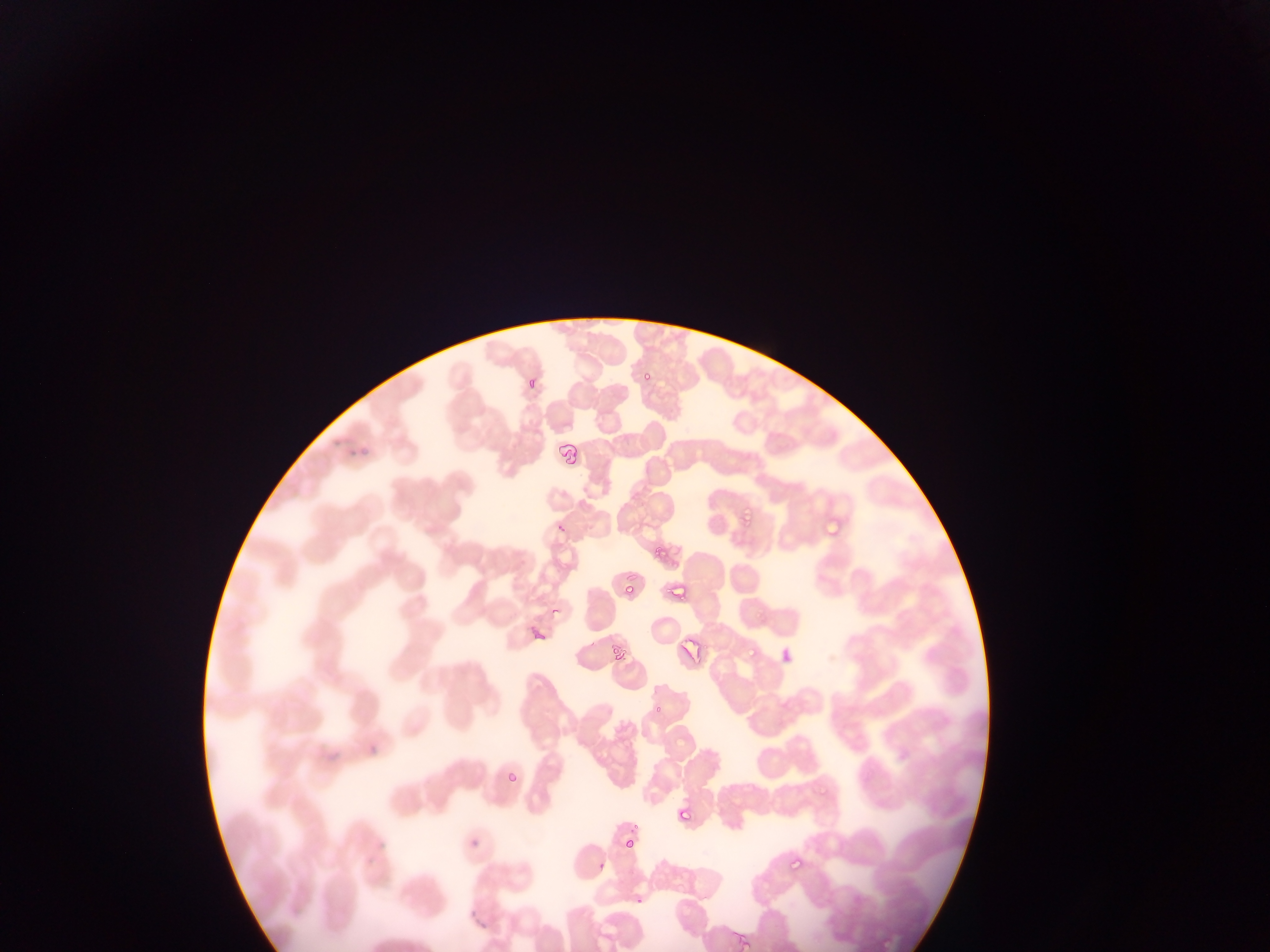

Approximate bounding boxes as [left, top, right, bottom] in pixels. Plasmodium parasite locations: [640, 368, 654, 378], [521, 382, 535, 398], [554, 438, 574, 473], [741, 503, 753, 531], [650, 543, 670, 565], [666, 582, 687, 603], [619, 586, 628, 601], [607, 642, 632, 659], [747, 643, 763, 666], [502, 759, 523, 781], [671, 793, 704, 827], [617, 826, 649, 853], [460, 831, 485, 850], [785, 848, 816, 873], [591, 849, 610, 874], [739, 931, 750, 952]. Collected in Ghana. Image is 1270×952 pixels. Photographed through a microscope with a mobile-phone camera. Thin blood film. Single field of view.